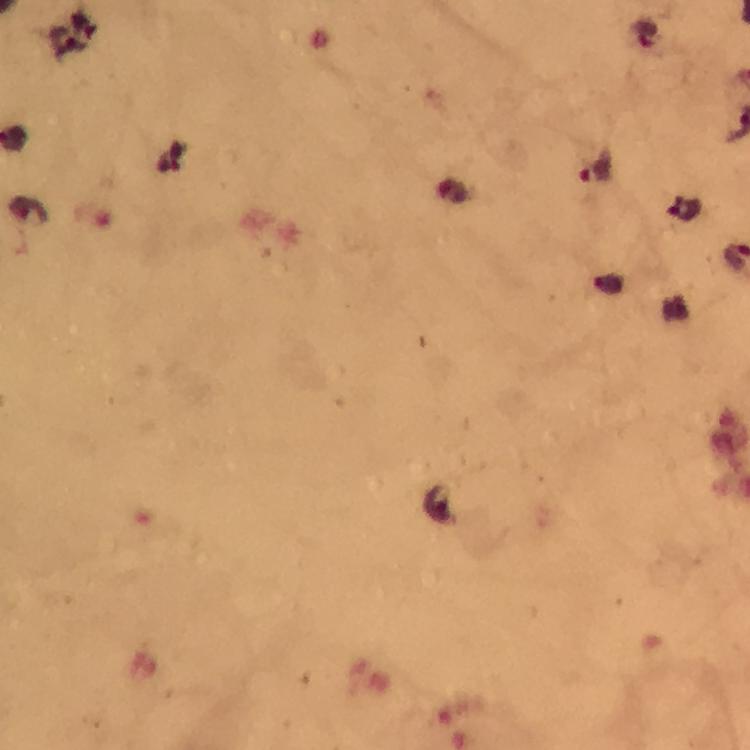

image_size: 750×750 pixels
magnification: 100x
stain: Giemsa
context: from a malaria diagnostic workup
capture: smartphone mounted on the microscope
preparation: thick smear
immersion_oil: used
cropped_from: a single field of view
plasmodium_parasite_locations: 'approximate centers as {x, y} in pixels: {646, 36}, {65, 41}, {597, 171}, {683, 207}'